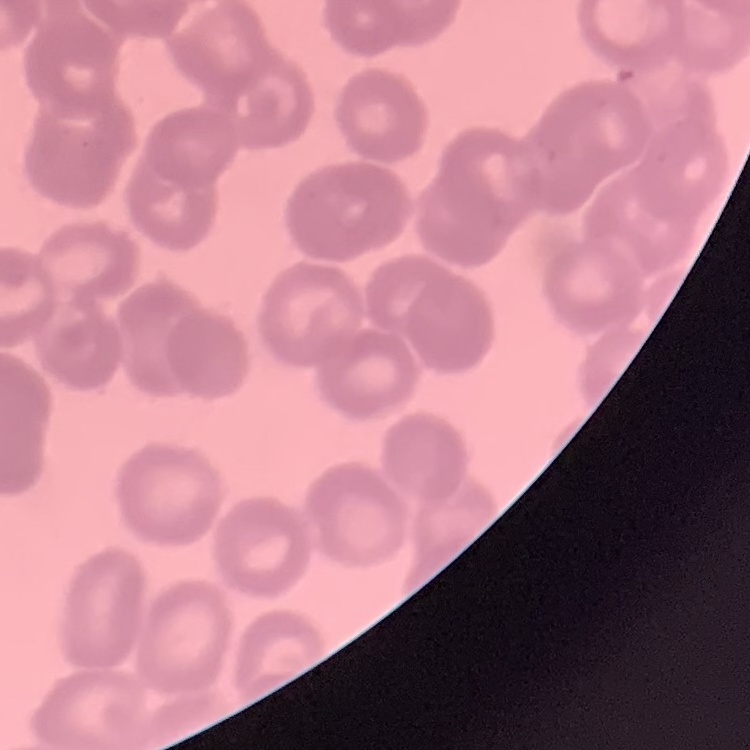

Summary:
  - Red blood cell morphology: rouleaux formation
  - Stain: Field's or Giemsa
  - Image type: one tile cut from a larger photomicrograph
  - Preparation: thin blood film